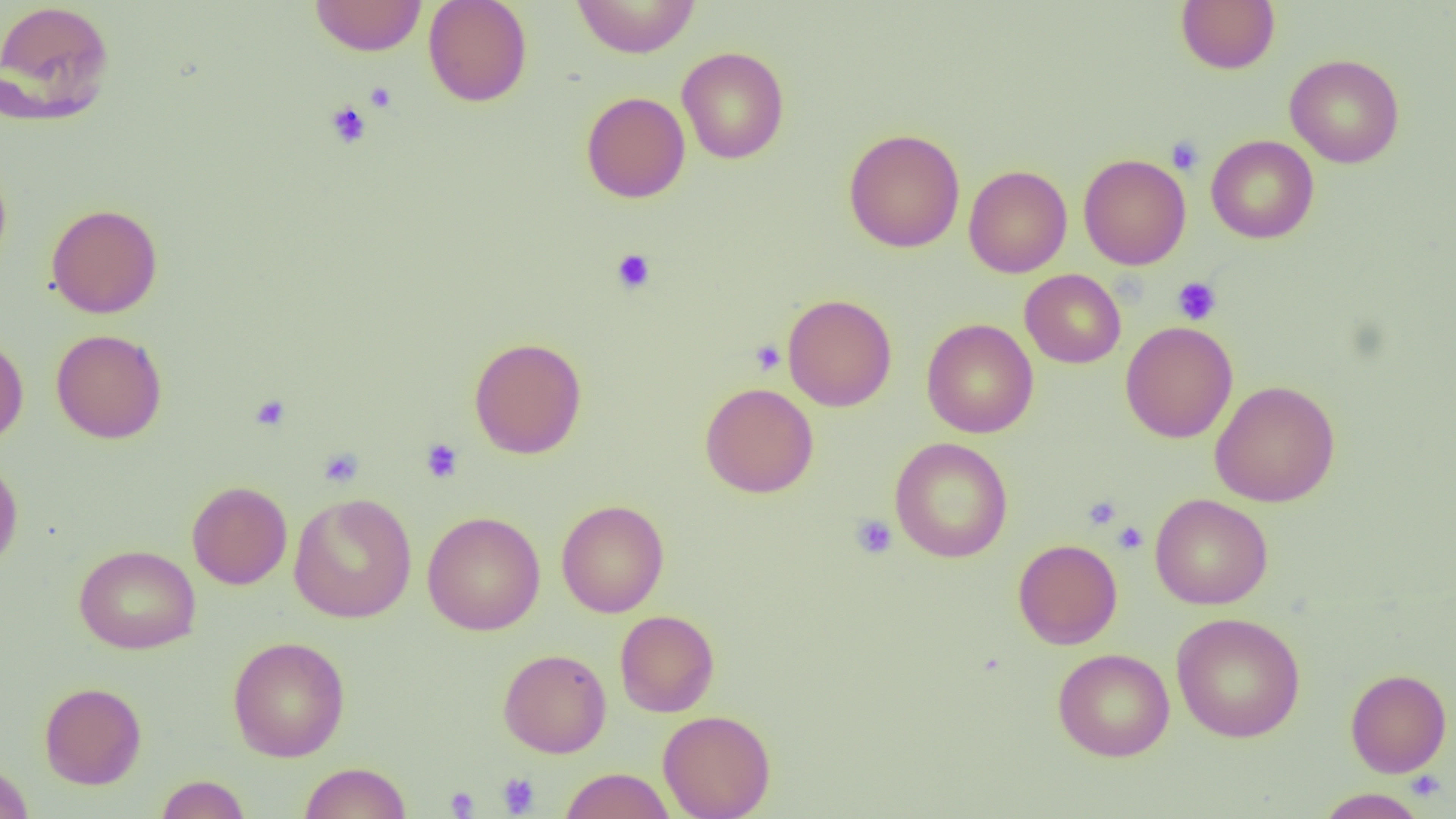

{
  "slide_level_diagnosis": "no evidence of blood parasites",
  "platelet_locations": "approximate bounding boxes as (x1, y1, x2, y2) in pixels: (364, 81, 397, 112), (326, 100, 371, 149), (1167, 136, 1204, 175), (611, 248, 656, 294), (1172, 277, 1221, 324), (750, 340, 786, 375), (250, 395, 290, 431), (420, 438, 464, 484), (318, 448, 363, 488), (1083, 495, 1121, 530), (851, 514, 898, 559), (1113, 522, 1148, 553), (1407, 771, 1447, 801), (497, 773, 540, 816), (444, 787, 480, 817)",
  "modality": "optical microscopy",
  "image_size": "1456×819 pixels",
  "preparation": "thin blood film",
  "magnification": "1000x",
  "uninfected_red_blood_cell_locations": "approximate bounding boxes as (x1, y1, x2, y2) in pixels: (309, 0, 427, 56), (423, 0, 532, 107), (571, 0, 701, 58), (1176, 0, 1280, 74), (0, 1, 116, 124), (677, 47, 789, 164), (1285, 54, 1404, 168), (581, 91, 691, 203), (843, 128, 965, 253), (1206, 135, 1319, 243), (1078, 154, 1191, 269), (0, 159, 13, 274), (964, 164, 1072, 278), (46, 203, 163, 318), (1020, 269, 1126, 368), (782, 294, 897, 412), (921, 318, 1038, 438), (1121, 321, 1238, 443), (51, 328, 167, 443), (0, 334, 28, 446), (468, 336, 586, 459), (1210, 380, 1340, 507), (700, 383, 819, 498), (889, 437, 1013, 563), (0, 455, 23, 574), (187, 481, 292, 589), (289, 493, 417, 623), (1150, 493, 1273, 610), (556, 500, 669, 617), (422, 511, 545, 635), (1013, 539, 1122, 649), (74, 545, 201, 654), (615, 610, 719, 717), (1171, 612, 1306, 743), (227, 636, 350, 762), (498, 648, 611, 758), (1053, 648, 1174, 761), (1345, 669, 1451, 777), (39, 681, 146, 789), (658, 710, 776, 819), (0, 761, 34, 819), (298, 761, 412, 819), (560, 768, 675, 818), (154, 775, 251, 818), (1315, 788, 1428, 818)",
  "field_of_view": "single"
}